Describe the morphology of the erythrocytes.
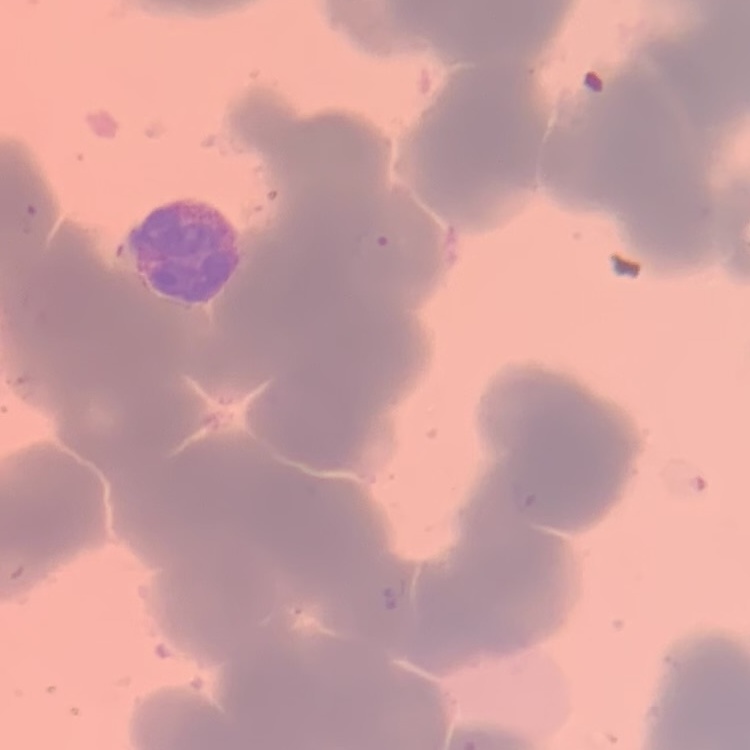

Rouleaux formation.

One tile cut from a larger photomicrograph. Thin peripheral smear. Stained with either Field's or Giemsa.